Comment on the morphology of the erythrocytes.
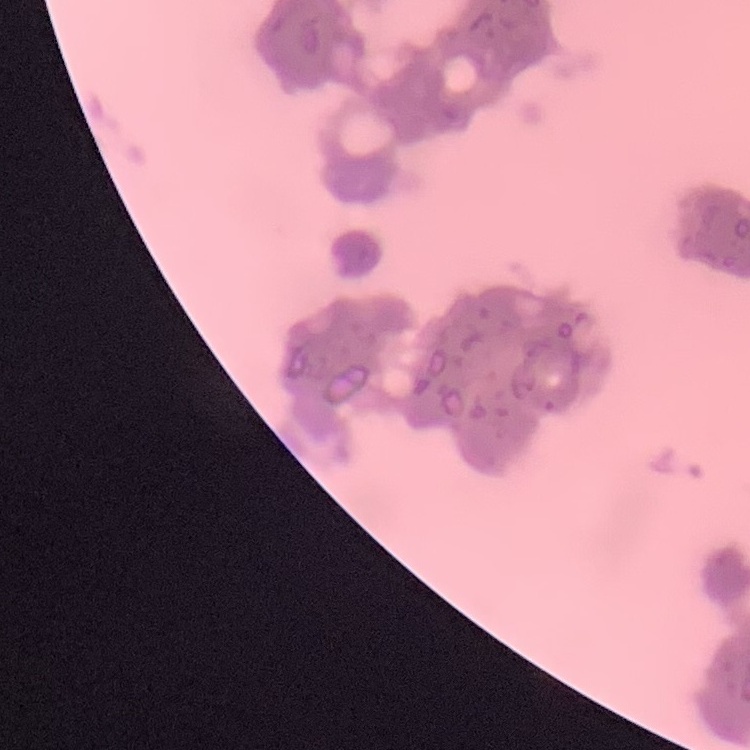
They show rouleaux formation.

Summary:
  - Stain: Field's or Giemsa
  - Image type: one tile cut from a larger photomicrograph
  - Preparation: thin peripheral smear